Give the position of every Plasmodium parasite.
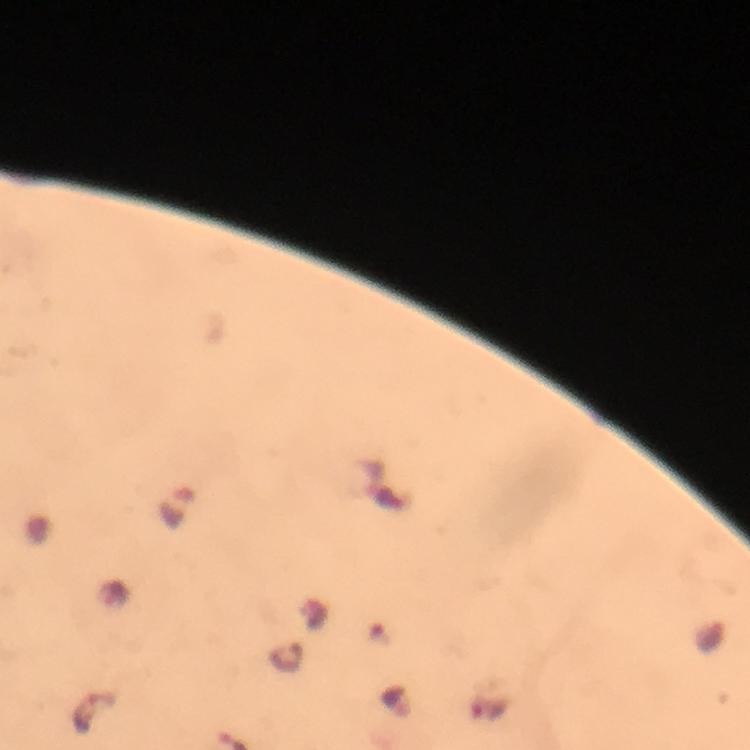
Approximate centers as [x, y] in pixels.
Plasmodium parasites: [95, 713].

context = from a malaria diagnostic workup
stain = Giemsa
immersion oil = applied
capture = smartphone photograph through a microscope
cropped from = one field of view
image size = 750×750 pixels
magnification = 100x
preparation = thick blood smear